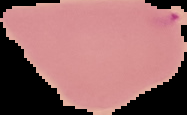
Summary:
  - Image type: segmented cell region on a black background
  - Preparation: thin blood smear
  - Result: no malaria parasites detected
  - Image size: 187×115 pixels